Outline each blood parasite and name the species.
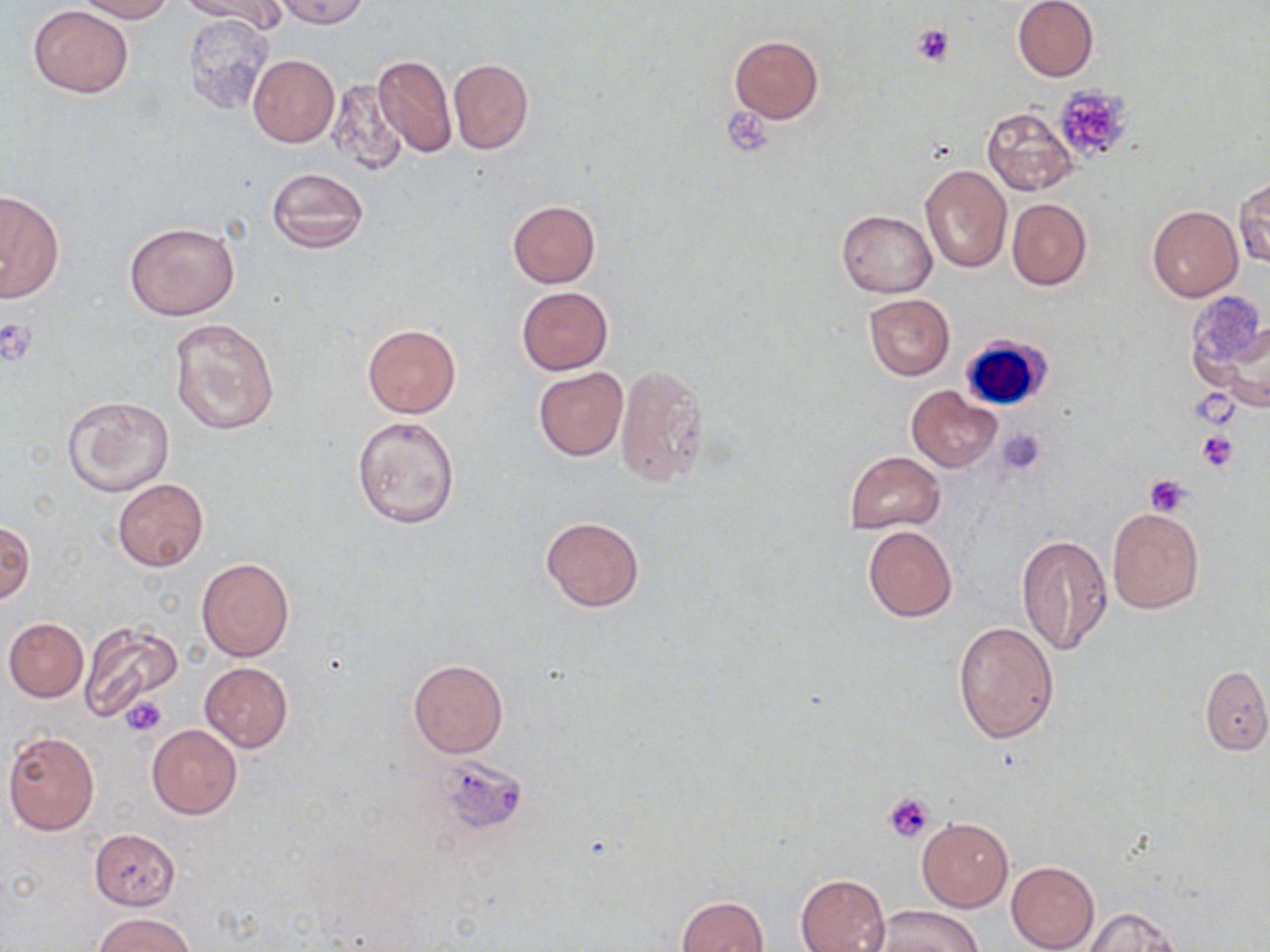
No blood parasites observed.

slide-level diagnosis = no evidence of blood parasites
uninfected red blood cell locations = approximate bounding boxes as [x1, y1, x2, y2] in pixels: [74, 0, 174, 22], [184, 0, 288, 35], [1011, 0, 1099, 82], [273, 1, 373, 27], [27, 4, 133, 97], [182, 14, 275, 117], [728, 35, 823, 122], [247, 53, 339, 147], [372, 53, 457, 160], [448, 59, 534, 155], [328, 79, 409, 177], [982, 106, 1078, 195], [919, 165, 1011, 273], [265, 167, 369, 257], [1234, 177, 1269, 268], [0, 191, 64, 302], [1007, 199, 1091, 290], [507, 200, 600, 288], [1147, 205, 1242, 302], [836, 210, 937, 296], [124, 221, 240, 320], [516, 287, 614, 375], [862, 293, 955, 381], [167, 316, 280, 436], [1210, 317, 1270, 414], [361, 324, 461, 418], [614, 365, 708, 489], [533, 368, 628, 461], [906, 386, 1001, 472], [62, 395, 175, 499], [351, 414, 461, 529], [843, 451, 946, 534], [112, 479, 208, 571], [1106, 508, 1203, 613], [540, 516, 644, 613], [1, 520, 34, 606], [862, 525, 957, 623], [1016, 534, 1113, 656], [196, 557, 294, 661], [2, 618, 88, 702], [77, 621, 182, 722], [953, 621, 1060, 742], [407, 658, 508, 758], [200, 661, 293, 752], [1200, 665, 1270, 754], [147, 725, 241, 819], [2, 730, 100, 835], [917, 817, 1012, 911], [88, 828, 181, 910], [1006, 860, 1098, 952], [795, 874, 890, 952], [676, 895, 769, 952], [866, 906, 983, 952], [1081, 906, 1183, 952], [95, 912, 196, 952]
magnification = 1000x
image size = 1270×952 pixels
stain = May-Grünwald-Giemsa
field of view = one of a larger specimen
modality = optical microscopy
white blood cell locations = approximate bounding boxes as [x1, y1, x2, y2] in pixels: [957, 334, 1052, 413]
preparation = thin blood film
platelet locations = approximate bounding boxes as [x1, y1, x2, y2] in pixels: [910, 22, 956, 67], [1052, 85, 1133, 163], [723, 112, 774, 152], [0, 315, 39, 367], [1191, 390, 1239, 430], [996, 427, 1047, 475], [1196, 429, 1238, 471], [1143, 475, 1194, 517], [121, 696, 167, 736], [435, 756, 529, 836], [883, 791, 936, 843]